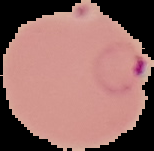

Summary:
  - Image type: cell region segmented out of the field of view; surrounding area masked to black
  - Image size: 154×151 pixels
  - Malaria status: parasitized
  - Preparation: thin blood smear